State the preparation type.
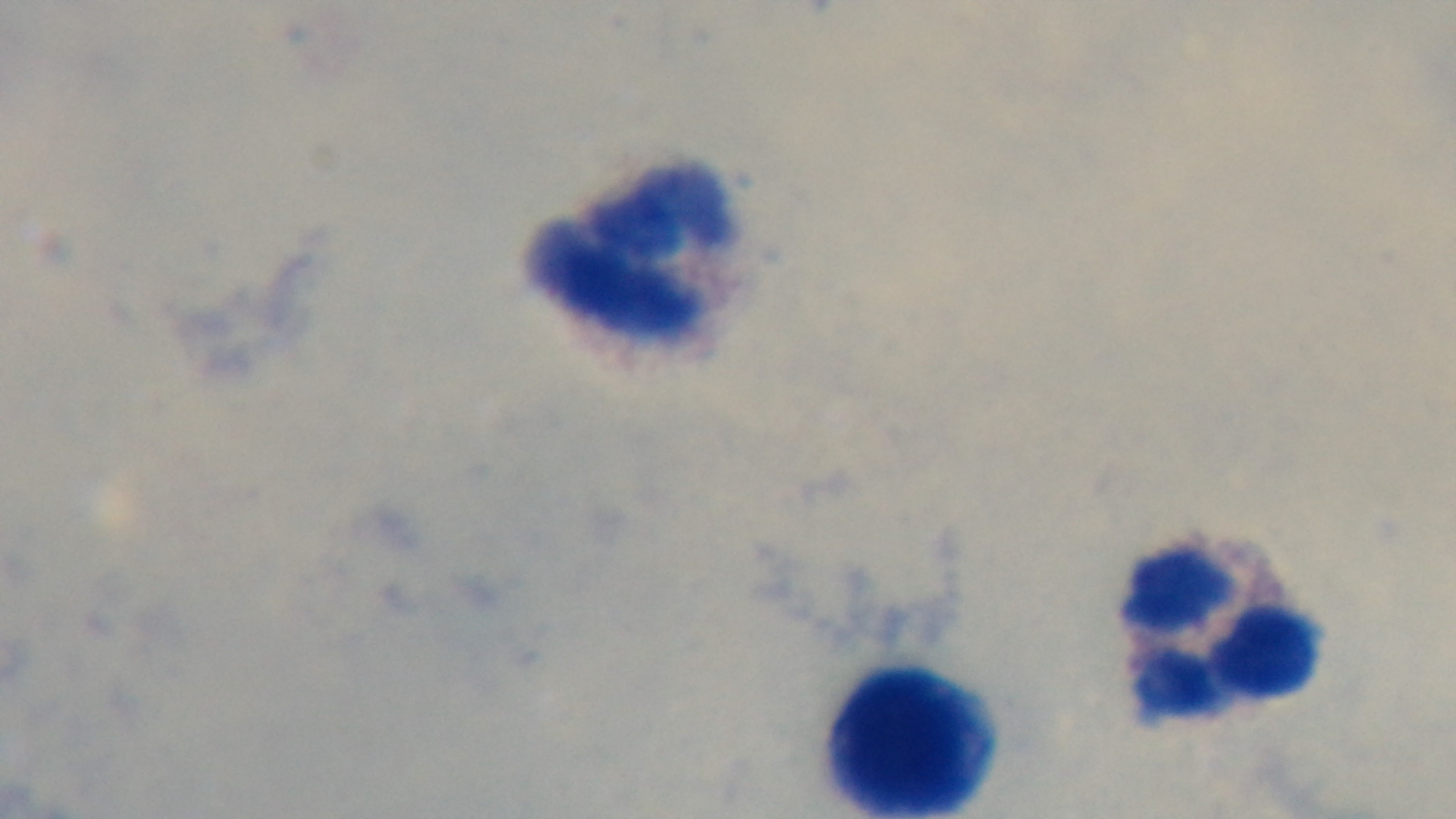
Thick.

Summary:
  - Capture: mounted 4K digital camera
  - Modality: light microscopy
  - Objective: 100x oil immersion
  - Field of view: single
  - Stain: Giemsa
  - Malaria status: negative